Classify this cell by malaria status.
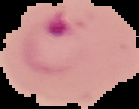
It is parasitized.

From a thin blood film. Segmented cell region on a black background. Image is 139×109 pixels.